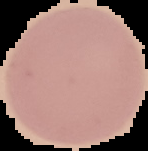
Summary:
  - Preparation: thin blood smear
  - Image size: 148×151 pixels
  - Image type: segmented cell region on a black background
  - Result: no malaria parasites seen